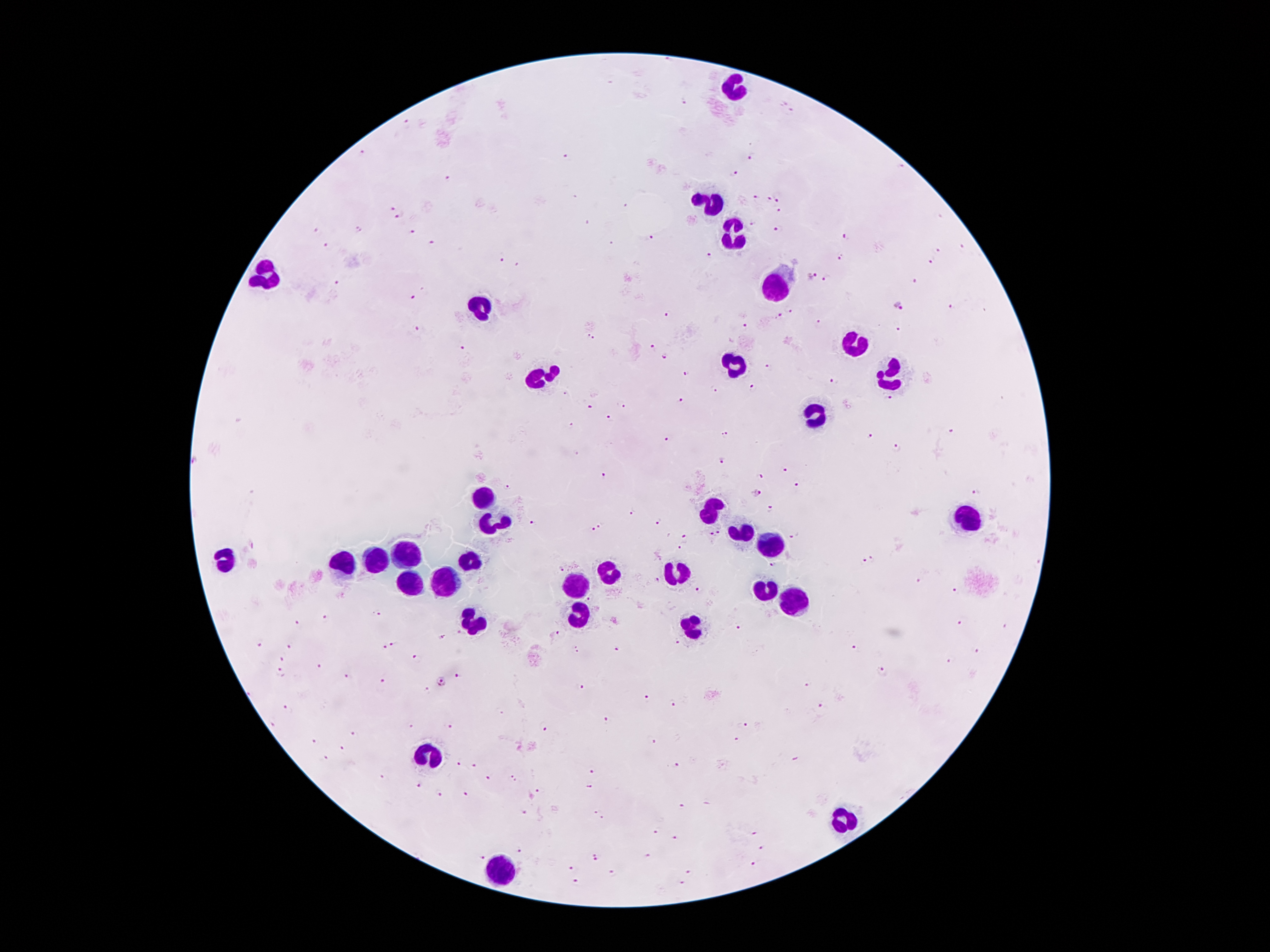
{
  "image_size": "1270×952 pixels",
  "stain": "Giemsa",
  "patient_malaria_status": "infected with Plasmodium falciparum",
  "magnification": "100x",
  "leukocyte_locations": "approximate centers as [x, y] in pixels: [736, 90], [710, 203], [732, 232], [267, 275], [774, 287], [486, 308], [853, 343], [736, 363], [534, 382], [891, 382], [820, 417], [482, 496], [708, 510], [962, 523], [496, 525], [736, 531], [771, 550], [410, 558], [379, 562], [227, 563], [469, 563], [343, 564], [677, 575], [605, 577], [446, 580], [412, 581], [572, 585], [763, 590], [786, 600], [578, 614], [475, 621], [694, 624], [427, 756], [847, 819], [501, 871]",
  "plasmodium_parasite_locations": "approximate centers as [x, y] in pixels: [670, 61], [684, 102], [792, 114], [407, 124], [361, 152], [751, 156], [565, 157], [901, 166], [735, 174], [448, 179], [576, 196], [754, 198], [769, 198], [778, 200], [627, 206], [392, 208], [778, 209], [399, 216], [752, 223], [780, 228], [359, 229], [318, 231], [413, 232], [846, 237], [651, 238], [432, 243], [611, 244], [327, 245], [963, 246], [937, 251], [711, 255], [841, 257], [500, 261], [929, 263], [516, 264], [812, 276], [826, 279], [914, 281], [336, 284], [411, 297], [897, 305], [949, 306], [788, 311], [668, 316], [779, 316], [818, 321], [743, 326], [896, 328], [417, 329], [590, 338], [462, 346], [653, 346], [664, 357], [769, 368], [687, 373], [834, 381], [752, 388], [713, 391], [562, 394], [887, 400], [681, 401], [621, 406], [590, 407], [609, 418], [571, 426], [949, 431], [724, 435], [870, 436], [665, 439], [898, 447], [722, 460], [784, 468], [603, 476], [761, 476], [798, 485], [506, 486], [756, 493], [975, 493], [769, 509], [630, 513], [533, 522], [657, 522], [602, 525], [593, 530], [718, 532], [710, 534], [792, 536], [685, 538], [680, 550], [874, 557], [864, 560], [1038, 562], [774, 564], [562, 567], [920, 580], [658, 582], [698, 590], [956, 591], [589, 600], [379, 614], [326, 618], [298, 622], [958, 623], [1003, 626], [737, 627], [555, 633], [442, 636], [676, 642], [260, 643], [395, 643], [290, 645], [385, 647], [854, 647], [577, 649], [616, 649], [976, 651], [416, 658], [283, 659], [948, 661], [318, 667], [880, 671], [281, 673], [347, 676], [458, 676], [383, 681], [439, 681], [808, 684], [580, 687], [427, 690], [646, 699], [672, 702], [820, 705], [289, 708], [609, 720], [273, 723], [747, 725], [448, 726], [412, 727], [543, 729], [352, 733], [652, 740], [736, 740], [314, 741], [344, 747], [327, 758], [796, 759], [460, 764], [475, 766], [676, 766], [592, 770], [381, 777], [513, 777], [489, 778], [416, 786], [589, 787], [539, 791], [440, 794], [466, 794], [709, 803], [682, 806], [525, 811], [594, 811], [601, 818], [657, 832], [756, 833], [676, 838], [763, 849], [518, 850], [480, 855], [595, 856], [649, 857], [752, 865], [571, 869], [688, 871], [614, 874], [681, 882]",
  "capture": "smartphone camera through the microscope eyepiece",
  "preparation": "thick peripheral-blood smear",
  "field_of_view": "one from this slide"
}